Assess the morphology of the erythrocytes.
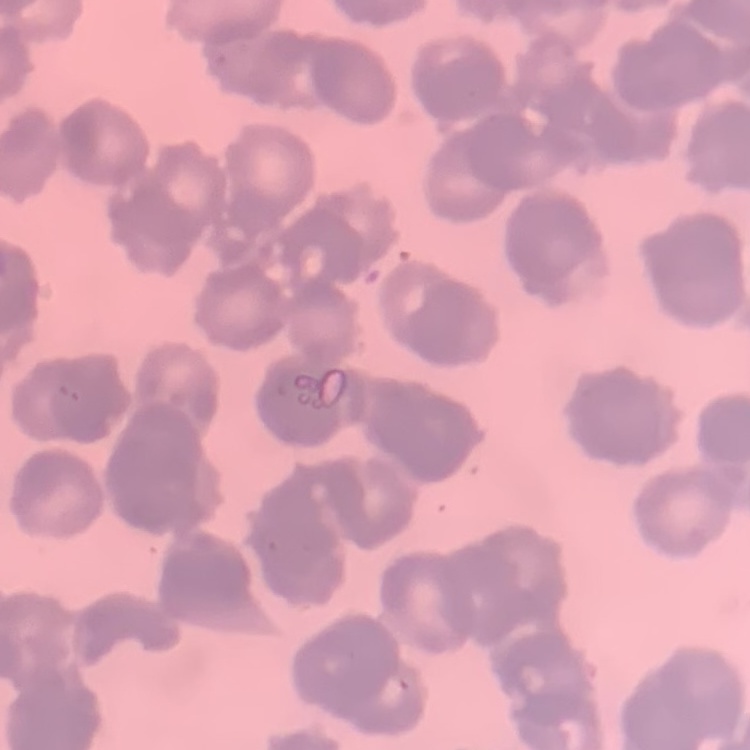
Rouleaux formation.

{
  "stain": "Field's or Giemsa",
  "image_type": "one tile cut from a larger photomicrograph",
  "preparation": "thin peripheral smear"
}